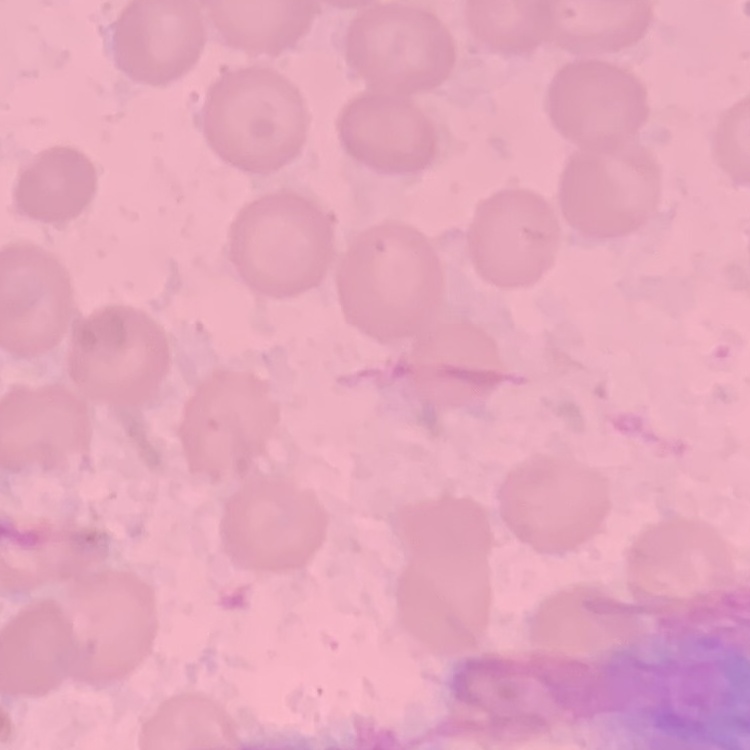

red blood cell morphology = no rouleaux formation
stain = Field's or Giemsa
image type = one tile cut from a larger photomicrograph
preparation = thin blood film